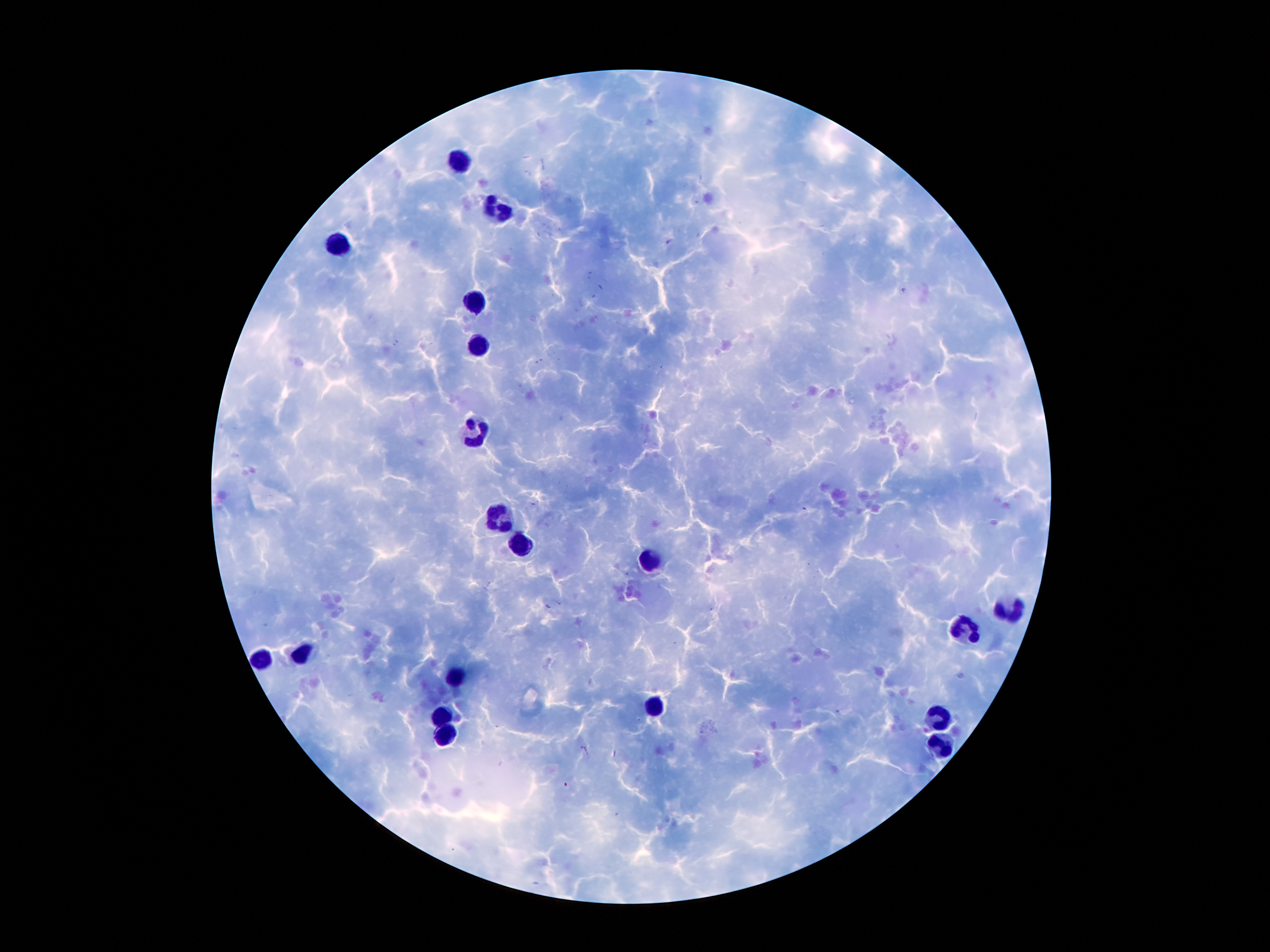
{
  "image_size": "1270×952 pixels",
  "leukocyte_locations": "approximate centers as {x, y} in pixels: {460, 160}, {499, 208}, {341, 243}, {476, 303}, {479, 348}, {478, 433}, {497, 517}, {522, 542}, {647, 560}, {1008, 608}, {967, 626}, {303, 651}, {264, 657}, {459, 675}, {655, 702}, {445, 713}, {935, 715}, {448, 736}, {942, 743}",
  "stain": "Giemsa",
  "magnification": "100x",
  "capture": "smartphone camera through the microscope eyepiece",
  "preparation": "thick blood smear",
  "patient_malaria_status": "infected with Plasmodium falciparum",
  "plasmodium_parasites": "not seen",
  "field_of_view": "single"
}